Comment on the morphology of the red blood cells.
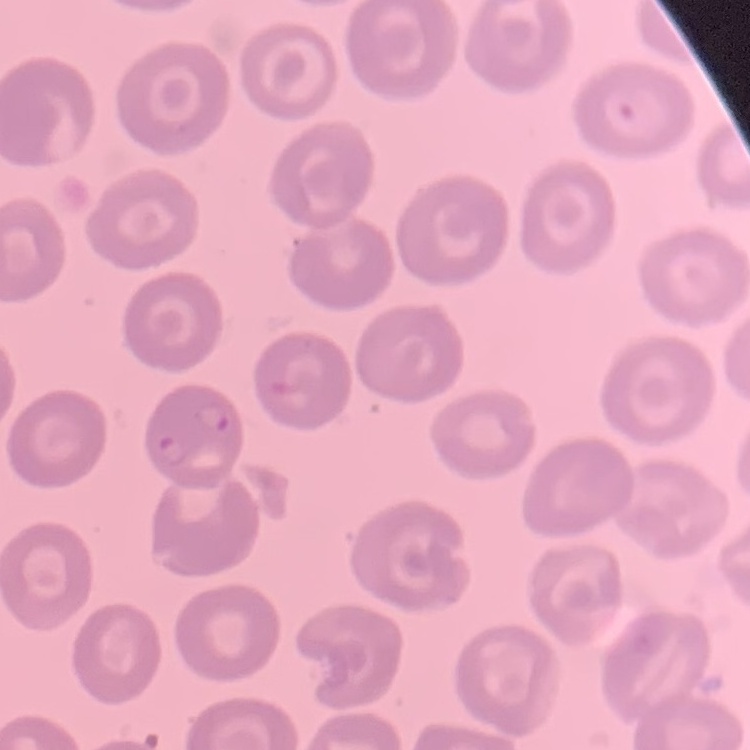

They show no rouleaux formation.

stain: Field's or Giemsa
preparation: thin peripheral smear
image_type: one tile cut from a larger photomicrograph